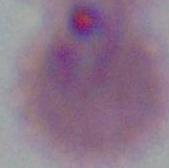
modality: micrograph
magnification: 400x or 1000x
identification: Plasmodium